Assess this cell for malaria.
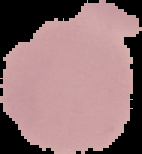

It is uninfected.

Image is 142×154 pixels. The area outside the segmented cell region is set to black. From a thin blood film.